Identify the preparation type.
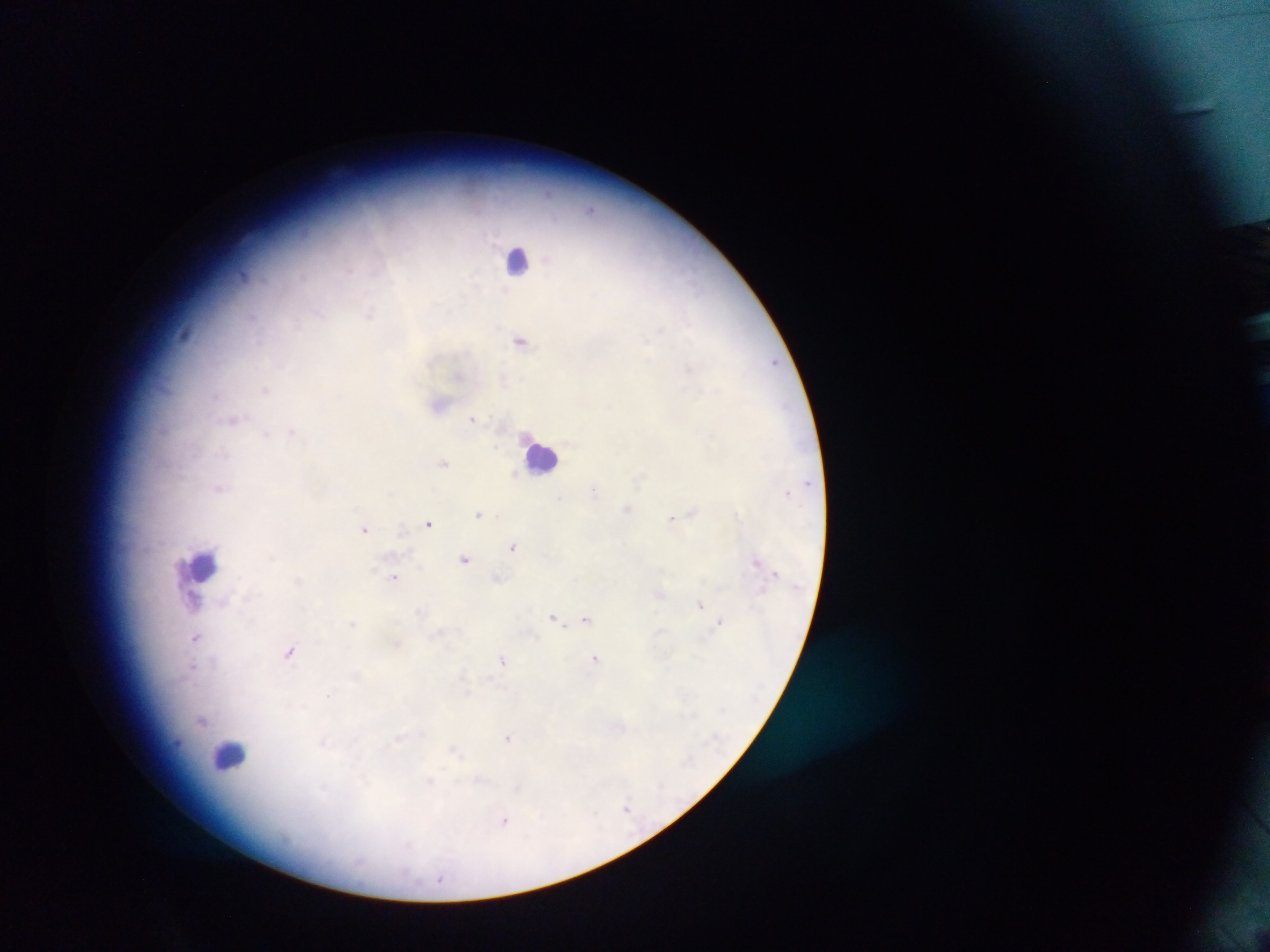

Thick blood smear.

Approximate centers as (x, y) in pixels.
Summary:
  - Plasmodium parasite locations: (521, 340), (774, 362), (689, 368), (266, 389), (439, 402), (234, 418), (473, 419), (292, 431), (444, 462), (788, 491), (628, 508), (694, 511), (480, 513), (673, 519), (430, 523), (365, 529), (514, 546), (466, 558), (758, 561), (394, 577), (498, 577), (661, 593), (193, 602), (701, 604), (553, 616), (586, 619), (720, 622), (353, 623), (196, 638), (291, 650), (596, 658), (504, 660), (204, 720), (508, 737), (627, 809), (505, 821)
  - Leukocyte locations: (519, 258), (541, 457), (202, 565), (228, 755)
  - Capture: mobile-phone photograph through a microscope
  - Country: Ghana
  - Field of view: single
  - Image size: 1270×952 pixels